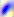
Toxoplasma gondii is seen. Photomicrograph. 400x magnification.